Locate and identify every blood parasite.
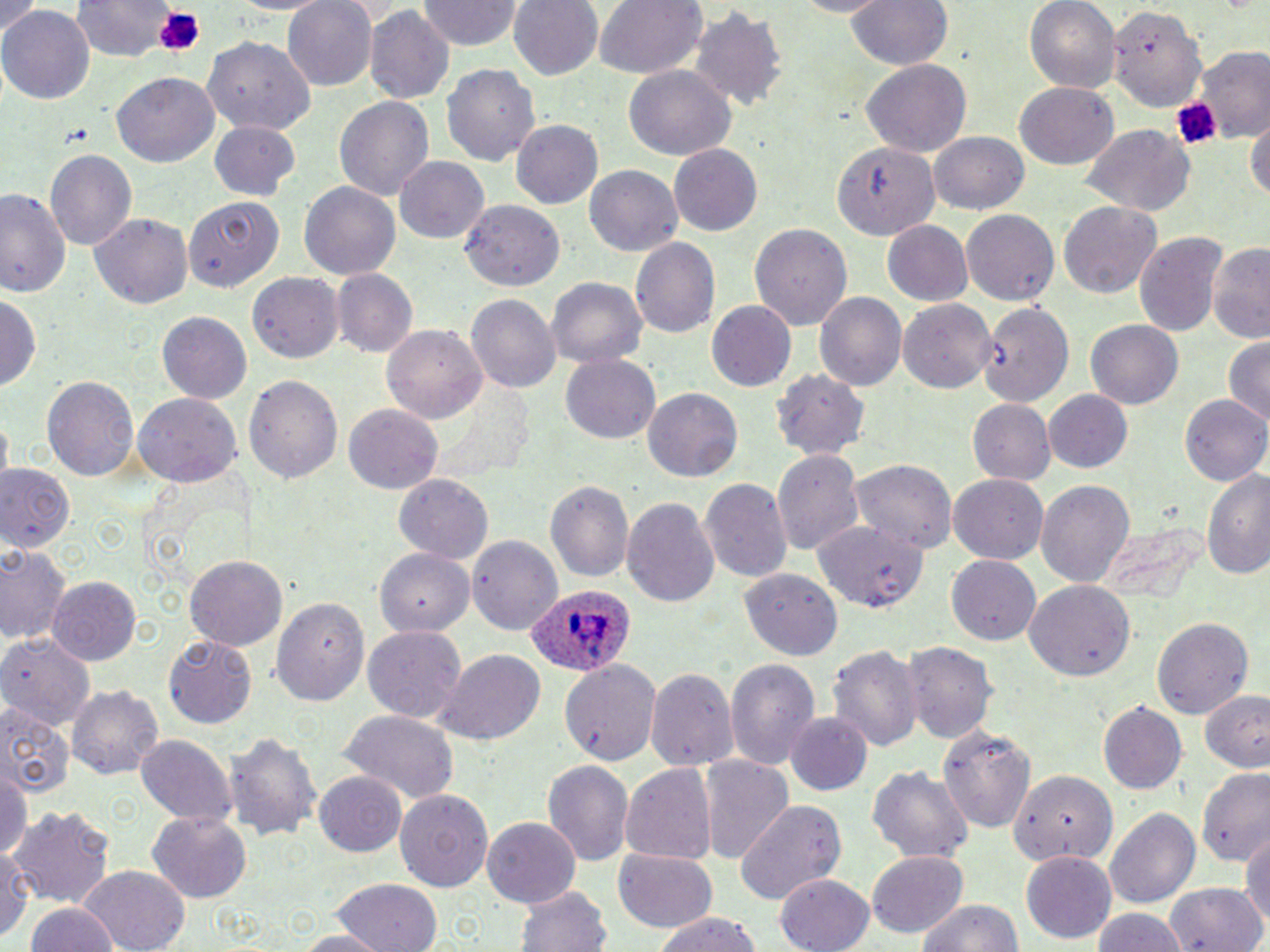
Approximate bounding boxes as (x1, y1, x2, y2) in pixels.
Plasmodium ovale-infected red blood cells: (525, 581, 636, 676).
No Plasmodium falciparum, Plasmodium malariae, Plasmodium vivax, Babesia divergens, or Trypanosoma brucei observed.

Summary:
  - Uninfected red blood cell locations: (71, 0, 173, 60), (225, 0, 332, 16), (280, 0, 377, 91), (420, 0, 521, 50), (509, 0, 603, 80), (593, 0, 706, 80), (844, 0, 953, 73), (1025, 0, 1119, 95), (1105, 0, 1209, 115), (0, 1, 44, 40), (0, 5, 92, 106), (364, 6, 453, 106), (690, 8, 788, 113), (204, 37, 315, 133), (1189, 48, 1269, 144), (443, 61, 543, 166), (861, 62, 971, 157), (625, 69, 733, 159), (112, 72, 218, 167), (1014, 83, 1119, 169), (334, 95, 435, 201), (1248, 108, 1269, 209), (512, 119, 605, 208), (210, 121, 300, 200), (1083, 125, 1195, 220), (929, 130, 1029, 214), (836, 142, 940, 239), (669, 144, 764, 236), (45, 149, 136, 253), (395, 157, 491, 243), (582, 165, 683, 256), (299, 181, 403, 281), (0, 188, 70, 298), (183, 196, 280, 293), (460, 201, 564, 292), (1056, 201, 1164, 301), (962, 209, 1058, 306), (91, 212, 194, 308), (881, 221, 974, 307), (749, 222, 851, 330), (1134, 229, 1229, 340), (631, 238, 720, 339), (1206, 240, 1269, 344), (332, 268, 417, 358), (248, 273, 341, 363), (546, 277, 647, 367), (815, 292, 906, 392), (1, 293, 41, 392), (467, 294, 560, 396), (898, 299, 996, 393), (979, 299, 1076, 409), (707, 301, 797, 393), (157, 311, 252, 404), (1085, 316, 1183, 408), (383, 324, 489, 421), (1223, 337, 1270, 429), (560, 354, 661, 443), (772, 365, 868, 459), (243, 374, 341, 485), (44, 376, 140, 483), (642, 388, 741, 483), (1043, 389, 1132, 473), (133, 394, 240, 488), (1181, 394, 1270, 484), (967, 399, 1056, 484), (344, 406, 441, 493), (772, 449, 866, 558), (850, 458, 958, 554), (1198, 462, 1270, 584), (0, 464, 75, 553), (392, 473, 495, 564), (949, 475, 1050, 563), (700, 478, 793, 584), (547, 479, 635, 584), (1036, 479, 1135, 590), (622, 495, 720, 611), (814, 520, 925, 607), (1092, 523, 1209, 607), (467, 534, 563, 632), (468, 534, 560, 635), (367, 541, 479, 641), (2, 544, 70, 646), (186, 555, 287, 650), (947, 556, 1040, 644), (738, 568, 842, 662), (49, 578, 139, 665), (1024, 580, 1133, 680), (270, 593, 371, 705), (1151, 615, 1253, 719), (362, 625, 466, 723), (0, 631, 96, 723), (164, 637, 257, 728), (905, 642, 995, 747), (829, 645, 922, 753), (433, 650, 546, 745), (723, 657, 820, 769), (559, 659, 661, 768), (645, 665, 738, 772), (67, 683, 164, 780), (1198, 687, 1270, 774), (1098, 702, 1187, 794), (0, 703, 73, 799), (339, 713, 460, 803), (786, 713, 873, 795), (938, 721, 1037, 834), (222, 729, 319, 839), (135, 734, 235, 824), (697, 755, 792, 861), (543, 761, 633, 865), (620, 762, 717, 865), (0, 766, 30, 861), (864, 767, 975, 865), (1198, 767, 1270, 867), (1007, 769, 1119, 865), (315, 773, 406, 857), (396, 791, 492, 891), (733, 798, 848, 910), (11, 803, 117, 908), (1104, 807, 1200, 909), (148, 811, 251, 902), (483, 817, 580, 907), (1240, 824, 1269, 939), (614, 847, 718, 932), (0, 848, 32, 943), (867, 851, 967, 938), (1022, 852, 1116, 942), (76, 866, 191, 951), (775, 873, 876, 952), (332, 879, 442, 951), (516, 882, 610, 952), (1164, 883, 1268, 952), (916, 896, 1026, 951), (25, 902, 118, 952), (1091, 906, 1187, 952), (654, 913, 764, 952), (286, 929, 394, 951)
  - Platelet locations: (152, 7, 207, 57), (1166, 94, 1222, 147), (65, 126, 92, 145)
  - Slide-level diagnosis: Plasmodium ovale
  - Image size: 1270×952 pixels
  - Field of view: single
  - Preparation: thin blood film
  - Magnification: 1000x
  - Modality: light microscopy
  - Stain: May-Grünwald-Giemsa